Identify the parasite.
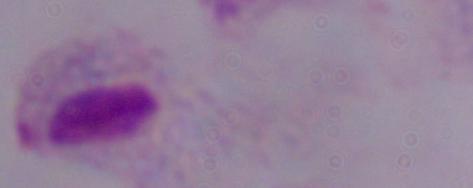

A trichomonad.

{
  "modality": "photomicrograph",
  "magnification": "1000x"
}